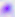

Toxoplasma gondii is seen. Captured at 400x magnification. Micrograph.